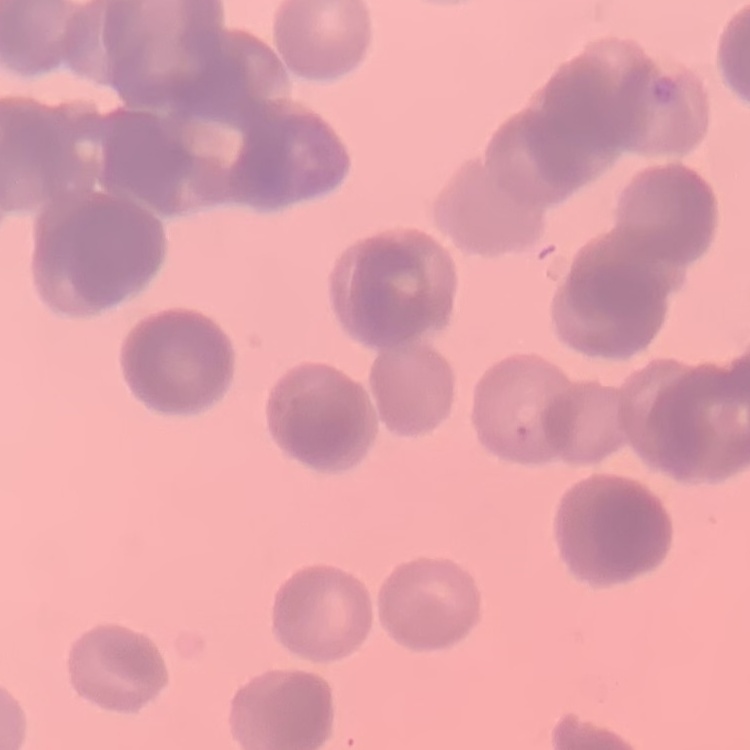
The red blood cells exhibit rouleaux formation. Square crop of a larger photomicrograph. Stained with either Field's or Giemsa. Thin blood smear.